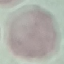
{
  "malaria_status": "uninfected",
  "stain": "Giemsa",
  "capture": "smartphone through the microscope eyepiece",
  "image_type": "automatically extracted cell patch, resized to 64 × 64 pixels",
  "preparation": "thin blood film"
}